Report the malaria status of this cell.
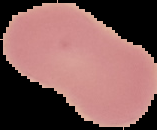

Uninfected.

image type = cell region segmented out of the field of view; surrounding area masked to black
image size = 157×130 pixels
preparation = thin blood smear